Identify the blood parasite species.
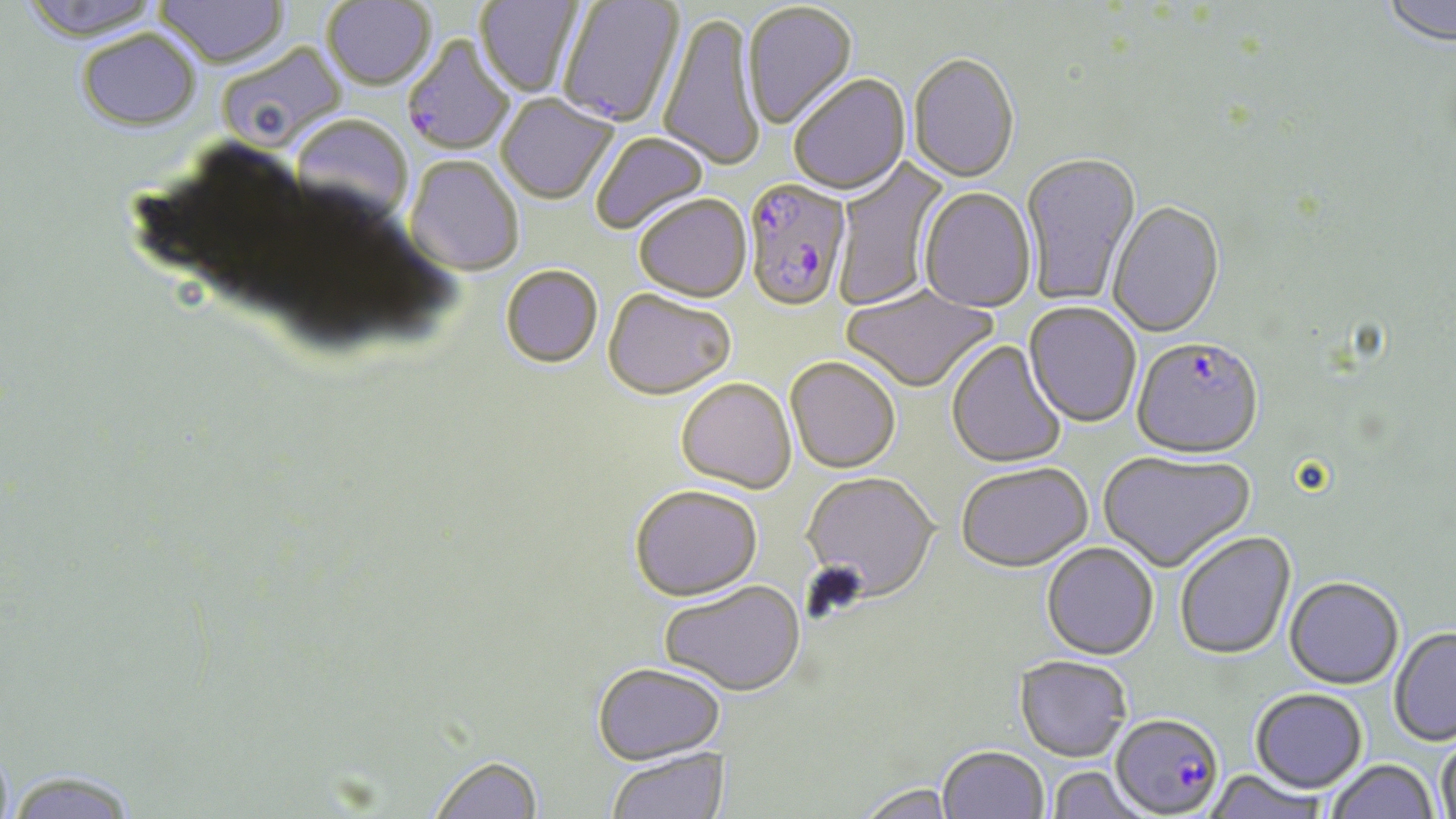
Plasmodium falciparum.

Summary:
  - Coordinate format: approximate bounding boxes as (x1,y1)-(x2,y2) corner pairs in pixels
  - Uninfected red blood cell locations: (16,0)-(166,44), (155,0)-(289,70), (475,0)-(584,98), (1381,0)-(1455,49), (322,1)-(436,92), (558,1)-(684,130), (744,3)-(859,132), (658,14)-(765,174), (77,32)-(201,133), (217,42)-(341,156), (908,56)-(1020,184), (788,76)-(911,197), (496,95)-(618,206), (290,117)-(412,229), (592,133)-(710,236), (1021,153)-(1142,306), (832,156)-(952,311), (405,157)-(523,277), (919,189)-(1037,315), (634,197)-(752,305), (1108,202)-(1225,340), (500,267)-(603,370), (841,284)-(998,395), (602,292)-(735,403), (1023,303)-(1141,429), (946,340)-(1067,470), (785,359)-(900,476), (676,380)-(797,496), (1098,451)-(1256,575), (955,464)-(1092,574), (801,474)-(939,604), (629,487)-(763,603), (1174,532)-(1296,661), (1040,543)-(1159,661), (1284,577)-(1404,689), (660,581)-(806,697), (1389,627)-(1456,747), (1013,655)-(1131,761), (592,664)-(726,766), (1250,689)-(1367,792), (1436,737)-(1456,819), (937,746)-(1049,819), (606,747)-(731,819), (427,754)-(544,819), (1325,759)-(1439,819), (1047,766)-(1151,818), (1203,771)-(1331,819), (5,772)-(139,819), (855,782)-(957,819)
  - Plasmodium falciparum-infected red blood cell locations: (402,37)-(516,156), (742,180)-(851,314), (1131,340)-(1265,461), (1111,718)-(1221,814)
  - Stain: May-Grünwald-Giemsa
  - Field of view: one of a larger specimen
  - Image size: 1456×819 pixels
  - Magnification: 1000x
  - Modality: optical microscopy
  - Preparation: thin blood film